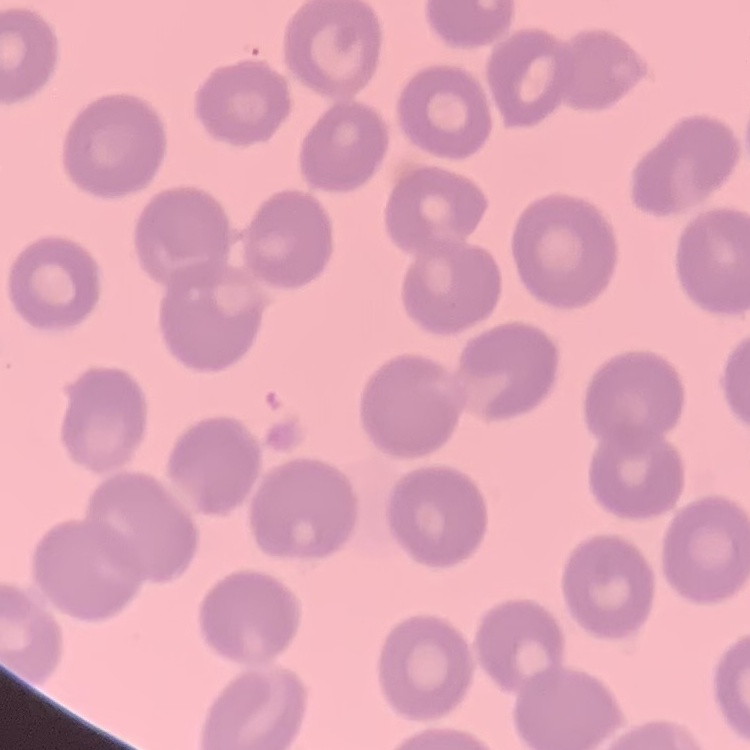
red blood cell morphology = no rouleaux formation
preparation = thin blood film
stain = Field's or Giemsa
image type = one tile cut from a larger photomicrograph